State which cell type is depicted.
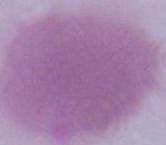
An erythrocyte.

Summary:
  - Magnification: 1000x
  - Modality: micrograph